Assess this cell for malaria.
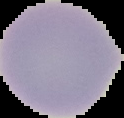
Uninfected.

Image is 124×118 pixels. From a thin blood film. Segmented cell region on a black background.